Give the position of every Plasmodium parasite visible.
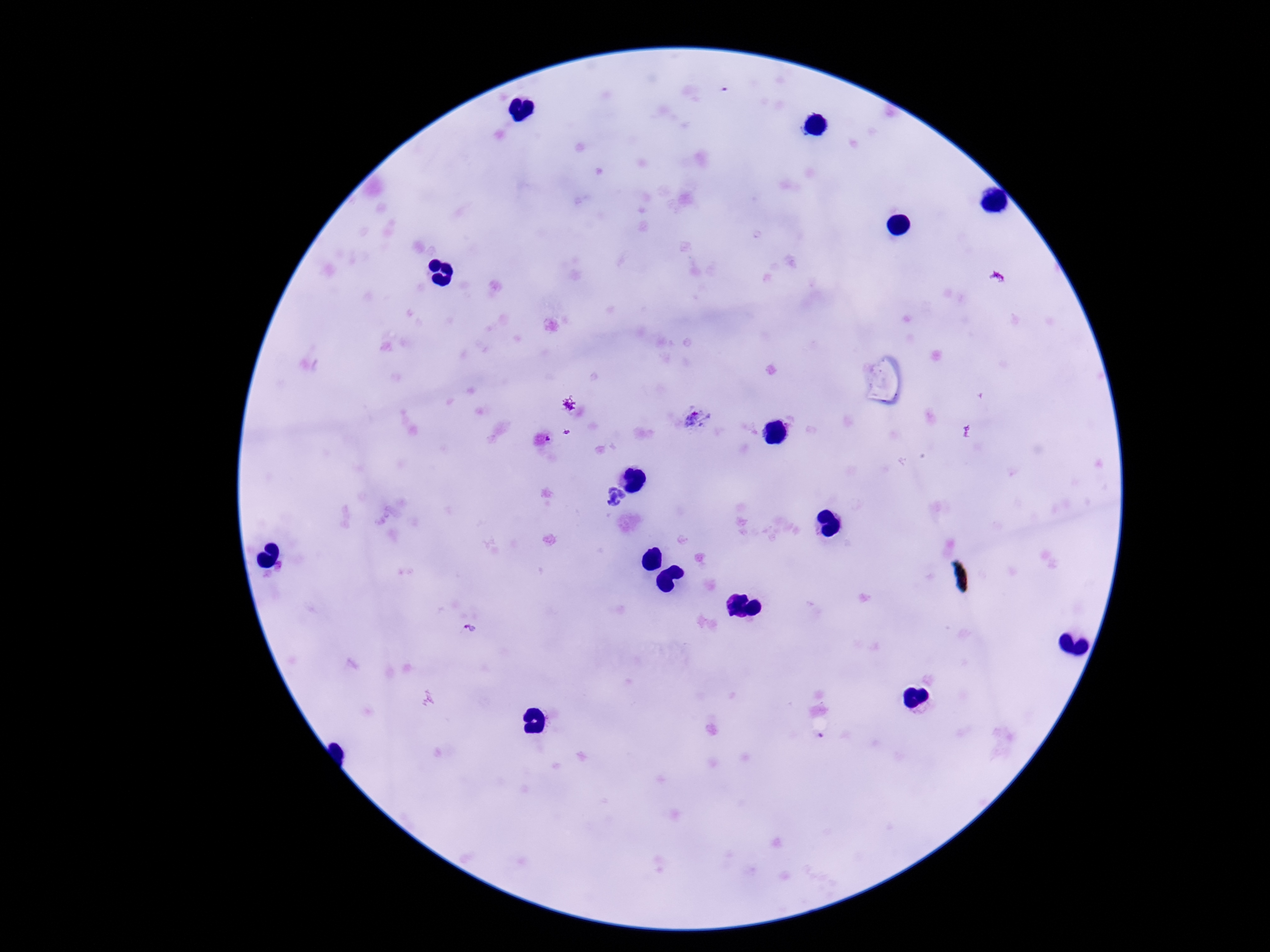

Approximate centers as [x, y] in pixels.
Plasmodium parasites: [696, 419], [569, 432], [472, 628], [820, 737].

field_of_view: one from this slide
patient_malaria_status: infected
image_size: 1270×952 pixels
magnification: 100x
capture: smartphone camera through the microscope eyepiece
preparation: thick blood film
stain: Giemsa